Outline each Trypanosoma brucei.
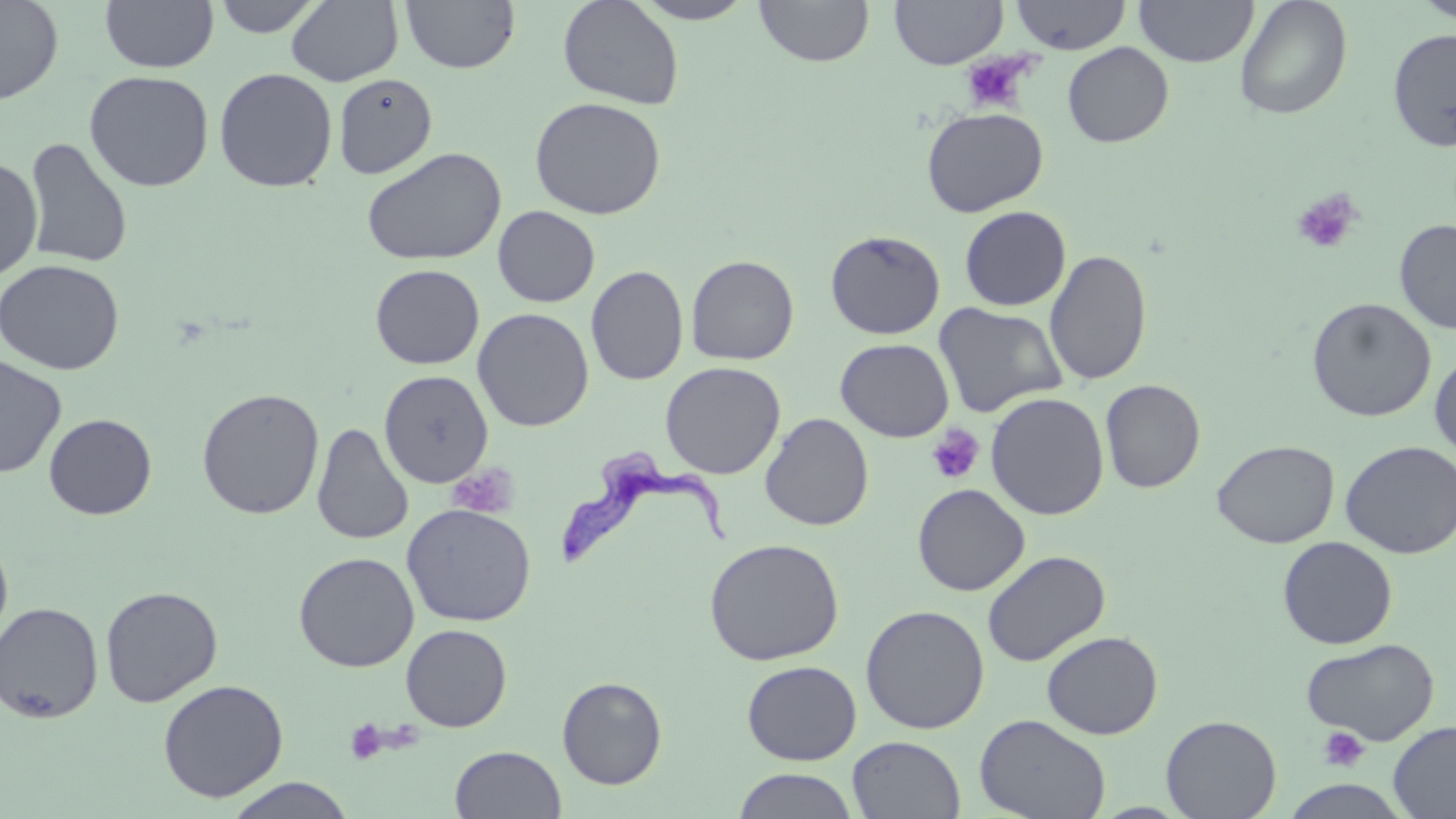
Approximate bounding boxes as [x1, y1, x2, y2] in pixels.
Trypanosoma brucei: [561, 444, 733, 569].

Platelet locations: [960, 53, 1033, 115], [1290, 188, 1364, 255], [926, 425, 985, 484], [447, 461, 518, 519], [345, 719, 387, 765], [1318, 725, 1370, 772]. Uninfected red blood cell locations: [0, 0, 64, 106], [100, 0, 219, 73], [211, 0, 325, 38], [286, 0, 403, 87], [400, 0, 520, 74], [557, 0, 684, 110], [632, 0, 757, 24], [754, 0, 875, 67], [889, 0, 1007, 69], [1008, 0, 1132, 54], [1134, 0, 1259, 67], [1235, 0, 1353, 119], [1414, 0, 1456, 23], [1387, 27, 1456, 152], [1062, 42, 1174, 147], [213, 67, 338, 192], [84, 70, 215, 192], [333, 73, 437, 179], [529, 96, 666, 220], [921, 106, 1048, 217], [23, 136, 134, 269], [361, 146, 506, 266], [0, 156, 43, 282], [492, 206, 600, 307], [959, 206, 1071, 311], [1394, 218, 1456, 335], [825, 229, 945, 340], [1044, 249, 1152, 386], [685, 255, 799, 365], [0, 259, 124, 375], [370, 264, 485, 369], [586, 265, 688, 385], [1306, 297, 1437, 422], [933, 303, 1067, 418], [472, 307, 595, 432], [835, 338, 954, 442], [1430, 351, 1456, 461], [0, 355, 66, 478], [660, 361, 786, 479], [379, 369, 493, 487], [1100, 379, 1206, 493], [196, 388, 325, 520], [985, 392, 1109, 520], [760, 412, 874, 531], [44, 413, 157, 520], [312, 422, 413, 546], [1212, 440, 1339, 548], [1340, 441, 1456, 558], [912, 483, 1030, 596], [401, 503, 536, 627], [0, 532, 14, 649], [1277, 536, 1398, 649], [704, 537, 844, 665], [981, 550, 1111, 667], [294, 552, 419, 672], [100, 585, 223, 707], [0, 601, 104, 723], [860, 605, 990, 734], [400, 624, 512, 732], [1042, 631, 1163, 739], [1302, 637, 1439, 745], [741, 660, 862, 765], [557, 676, 667, 789], [157, 679, 289, 802], [974, 714, 1111, 819], [1161, 714, 1282, 819], [1388, 721, 1456, 818], [847, 736, 965, 819], [451, 745, 567, 818], [732, 768, 859, 819], [223, 777, 358, 818]. Slide-level diagnosis: Trypanosoma brucei. 1000x magnification. Single field of view. Optical microscopy. Thin blood film. May-Grünwald-Giemsa-stained preparation. Image is 1456×819 pixels.